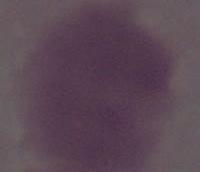

Captured at 1000x magnification. An erythrocyte is seen. Photomicrograph.